Identify the blood parasite species.
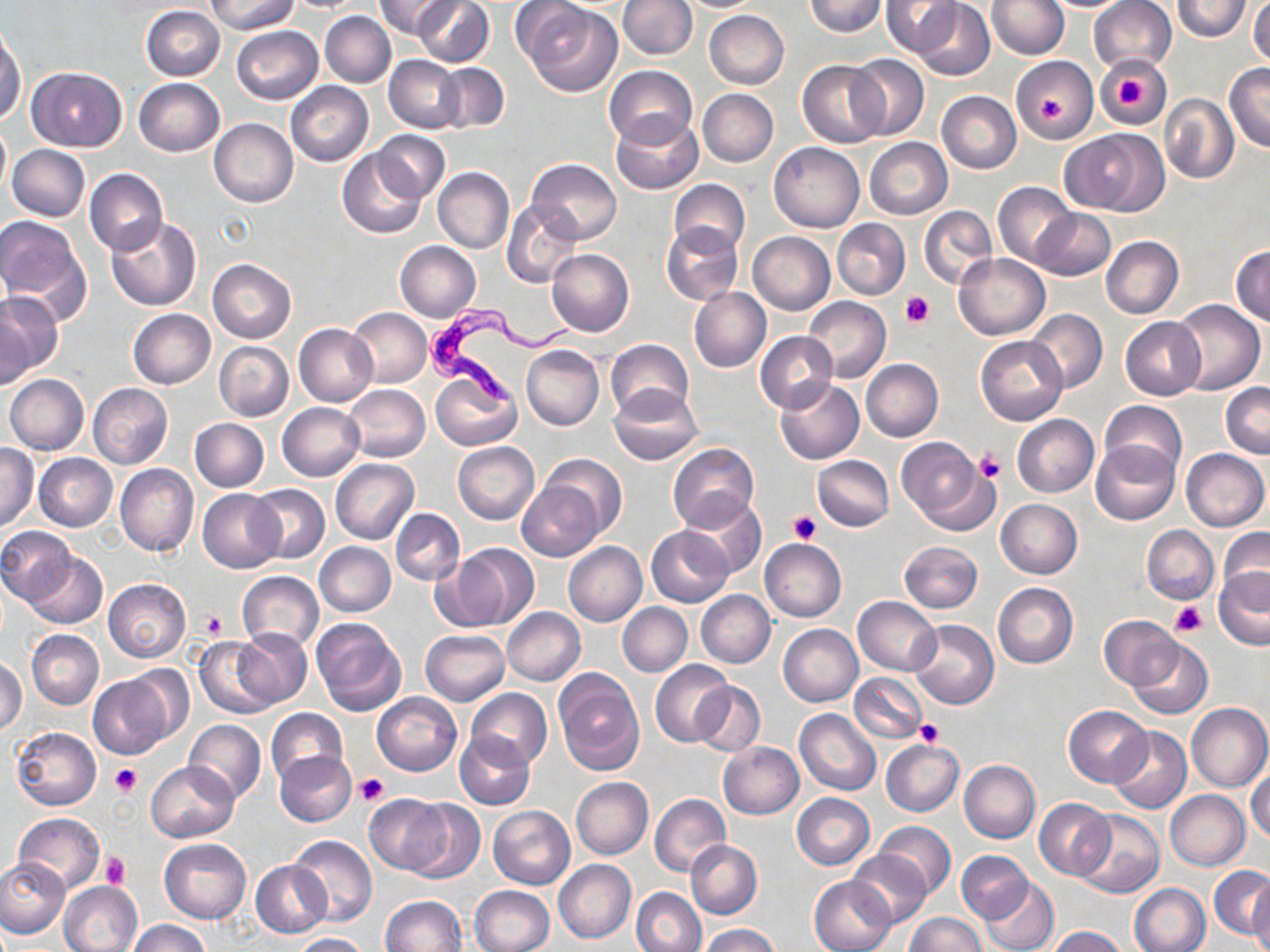
Trypanosoma brucei.

Summary:
  - Coordinate format: approximate bounding boxes as (x1, y1, x2, y2) in pixels
  - Uninfected red blood cell locations: (208, 0, 297, 34), (374, 0, 454, 41), (413, 0, 494, 67), (618, 0, 697, 60), (802, 0, 888, 36), (987, 0, 1069, 59), (1088, 0, 1176, 74), (1171, 0, 1253, 40), (1249, 0, 1270, 67), (881, 1, 961, 56), (914, 3, 994, 79), (521, 4, 622, 98), (141, 6, 226, 80), (704, 10, 789, 88), (320, 11, 396, 88), (231, 26, 323, 103), (1, 28, 25, 122), (847, 54, 928, 141), (1095, 55, 1171, 128), (384, 56, 463, 132), (1011, 56, 1099, 142), (798, 60, 889, 148), (436, 63, 511, 133), (1225, 64, 1270, 151), (605, 66, 697, 148), (29, 67, 126, 151), (134, 78, 224, 156), (286, 81, 373, 167), (698, 89, 778, 166), (937, 91, 1021, 172), (1161, 94, 1239, 183), (610, 114, 703, 195), (209, 119, 298, 207), (0, 123, 10, 197), (1059, 129, 1167, 215), (373, 130, 449, 202), (865, 138, 952, 219), (769, 142, 864, 232), (8, 144, 90, 222), (338, 148, 428, 239), (527, 158, 621, 245), (433, 167, 513, 254), (85, 168, 168, 255), (669, 180, 750, 257), (993, 181, 1079, 269), (502, 200, 583, 288), (919, 206, 996, 288), (1030, 209, 1115, 280), (0, 216, 86, 310), (107, 217, 201, 310), (833, 219, 909, 299), (661, 223, 744, 306), (748, 232, 834, 314), (1101, 237, 1183, 319), (395, 241, 481, 322), (1230, 246, 1269, 327), (546, 248, 634, 336), (953, 253, 1050, 341), (207, 259, 295, 342), (689, 286, 771, 373), (0, 290, 63, 380), (803, 296, 890, 383), (1169, 299, 1264, 396), (347, 307, 432, 387), (128, 309, 215, 388), (0, 310, 31, 394), (1027, 310, 1107, 392), (1120, 317, 1206, 400), (294, 324, 378, 406), (755, 331, 839, 412), (975, 335, 1067, 426), (606, 338, 694, 420), (214, 341, 293, 421), (520, 345, 604, 429), (861, 360, 942, 441), (431, 369, 521, 451), (4, 373, 88, 455), (774, 378, 864, 464), (1221, 382, 1270, 458), (88, 383, 172, 468), (343, 384, 431, 462), (607, 385, 703, 465), (1099, 400, 1187, 482), (278, 403, 364, 480), (1012, 414, 1098, 496), (190, 418, 269, 492), (895, 436, 992, 529), (453, 442, 540, 523), (668, 442, 759, 531), (1090, 442, 1179, 525), (0, 444, 38, 531), (1181, 449, 1268, 531), (34, 453, 117, 531), (540, 453, 625, 540), (812, 456, 893, 532), (330, 459, 418, 544), (116, 464, 198, 557), (516, 480, 604, 560), (248, 484, 328, 565), (197, 488, 285, 573), (679, 494, 767, 581), (995, 498, 1082, 578), (391, 508, 465, 585), (1142, 525, 1218, 604), (645, 526, 735, 607), (0, 527, 76, 604), (1217, 527, 1270, 607), (759, 538, 846, 622), (900, 540, 982, 613), (564, 541, 647, 626), (314, 542, 396, 616), (439, 543, 540, 632), (25, 552, 106, 630), (1212, 566, 1270, 650), (237, 571, 323, 653), (103, 579, 190, 663), (993, 583, 1077, 668), (696, 590, 775, 668), (854, 596, 940, 676), (617, 602, 692, 676), (503, 607, 586, 684), (1099, 615, 1179, 689), (310, 618, 406, 718), (909, 620, 999, 709), (778, 624, 862, 706), (235, 628, 312, 706), (420, 629, 509, 705), (27, 630, 103, 709), (193, 636, 281, 717), (1128, 637, 1212, 719), (1, 657, 26, 735), (651, 660, 734, 747), (123, 666, 194, 748), (553, 670, 643, 774), (849, 673, 927, 743), (88, 674, 171, 759), (690, 681, 765, 757), (466, 688, 553, 769), (371, 693, 462, 776), (1185, 702, 1270, 793), (1064, 705, 1151, 787), (264, 708, 347, 787), (794, 708, 880, 795), (185, 720, 267, 802), (1107, 726, 1191, 813), (12, 728, 101, 809), (455, 731, 536, 810), (881, 739, 963, 816), (717, 742, 803, 819), (275, 750, 357, 828), (147, 760, 239, 842), (958, 760, 1040, 842), (1247, 767, 1270, 843), (571, 777, 654, 859), (1165, 789, 1251, 870), (791, 792, 875, 869), (364, 793, 452, 875), (649, 793, 731, 877), (1035, 797, 1114, 880), (404, 799, 484, 884), (488, 805, 576, 889), (1074, 810, 1164, 899), (12, 813, 106, 895), (873, 822, 957, 898), (288, 834, 377, 928), (159, 838, 252, 923), (686, 840, 763, 918), (849, 850, 930, 929), (957, 851, 1032, 922), (0, 857, 71, 938), (251, 859, 328, 937), (554, 859, 637, 944), (1209, 865, 1270, 940), (809, 875, 896, 952), (981, 877, 1057, 952), (1249, 877, 1270, 952), (58, 880, 142, 952), (1128, 882, 1210, 952), (470, 885, 554, 952), (632, 887, 706, 952), (380, 895, 466, 951), (905, 913, 987, 952), (126, 919, 210, 952), (700, 924, 780, 952), (1045, 925, 1128, 952), (290, 933, 369, 951)
  - Platelet locations: (1116, 75, 1151, 110), (1035, 93, 1065, 127), (900, 292, 934, 328), (973, 448, 1005, 485), (789, 510, 821, 543), (1170, 601, 1206, 637), (200, 610, 228, 638), (917, 719, 944, 745), (110, 763, 143, 796), (356, 774, 388, 805), (101, 851, 130, 888)
  - Trypanosoma brucei locations: (419, 300, 582, 406)
  - Magnification: 1000x
  - Field of view: one of a larger specimen
  - Modality: light microscopy
  - Stain: May-Grünwald-Giemsa
  - Preparation: thin blood smear
  - Image size: 1270×952 pixels